Assess this cell for malaria.
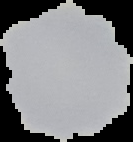

Uninfected.

Summary:
  - Image type: segmented cell region on a black background
  - Image size: 133×142 pixels
  - Preparation: thin blood smear